Give the position of every Plasmodium parasite.
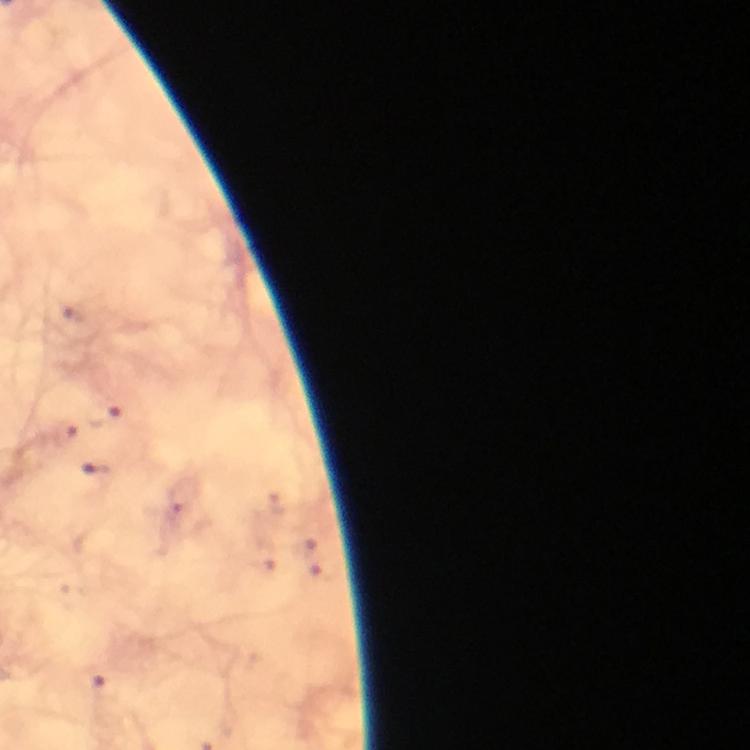
Approximate centers as [x, y] in pixels.
Plasmodium parasites: [106, 413], [64, 433], [105, 686].

Summary:
  - Cropped from: a single field of view
  - Context: from a diagnostic examination for malaria
  - Immersion oil: used
  - Magnification: 100x
  - Stain: Giemsa
  - Capture: smartphone camera through the microscope
  - Image size: 750×750 pixels
  - Preparation: thick blood film